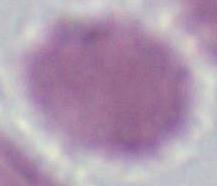

An erythrocyte is seen. Captured at 1000x magnification. Photomicrograph.